Report the malaria status of this cell.
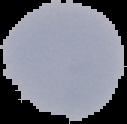
Uninfected.

preparation = thin blood smear
image size = 127×124 pixels
image type = segmented cell region on a black background